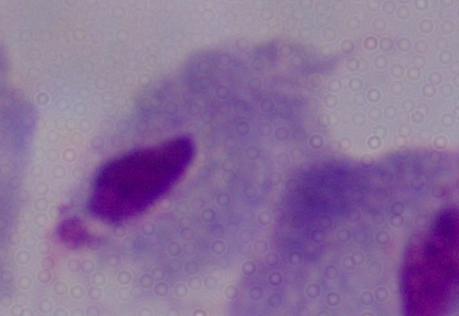

{
  "magnification": "1000x",
  "identification": "trichomonad",
  "modality": "micrograph"
}